Give the position of every Plasmodium parasite.
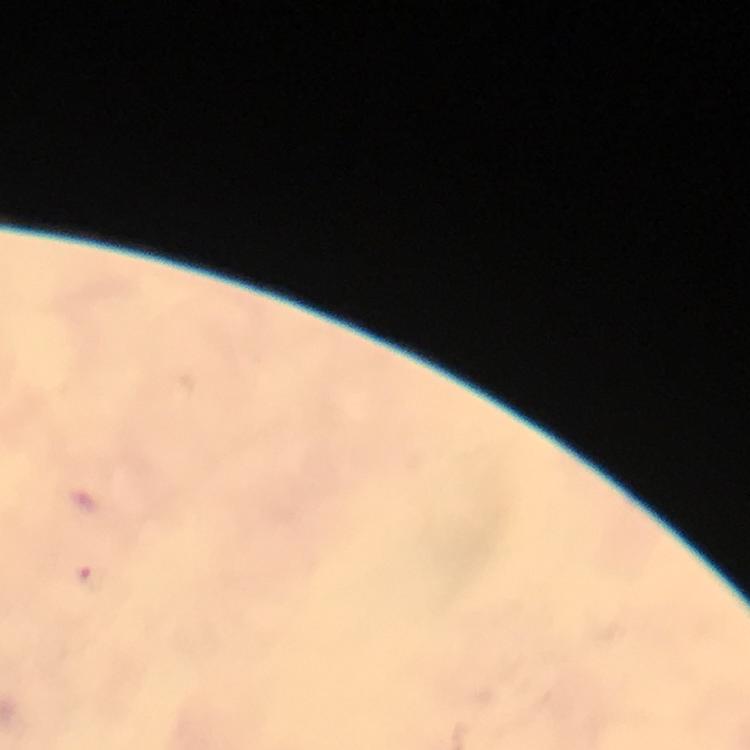
Approximate centers as {x, y} in pixels.
Plasmodium parasites: {91, 578}.

Giemsa stain. Image is 750×750 pixels. At 100x magnification. Thick blood film. From a diagnostic examination for malaria. Smartphone photograph taken through a microscope. Immersion oil was used. Cropped region of a single field of view.